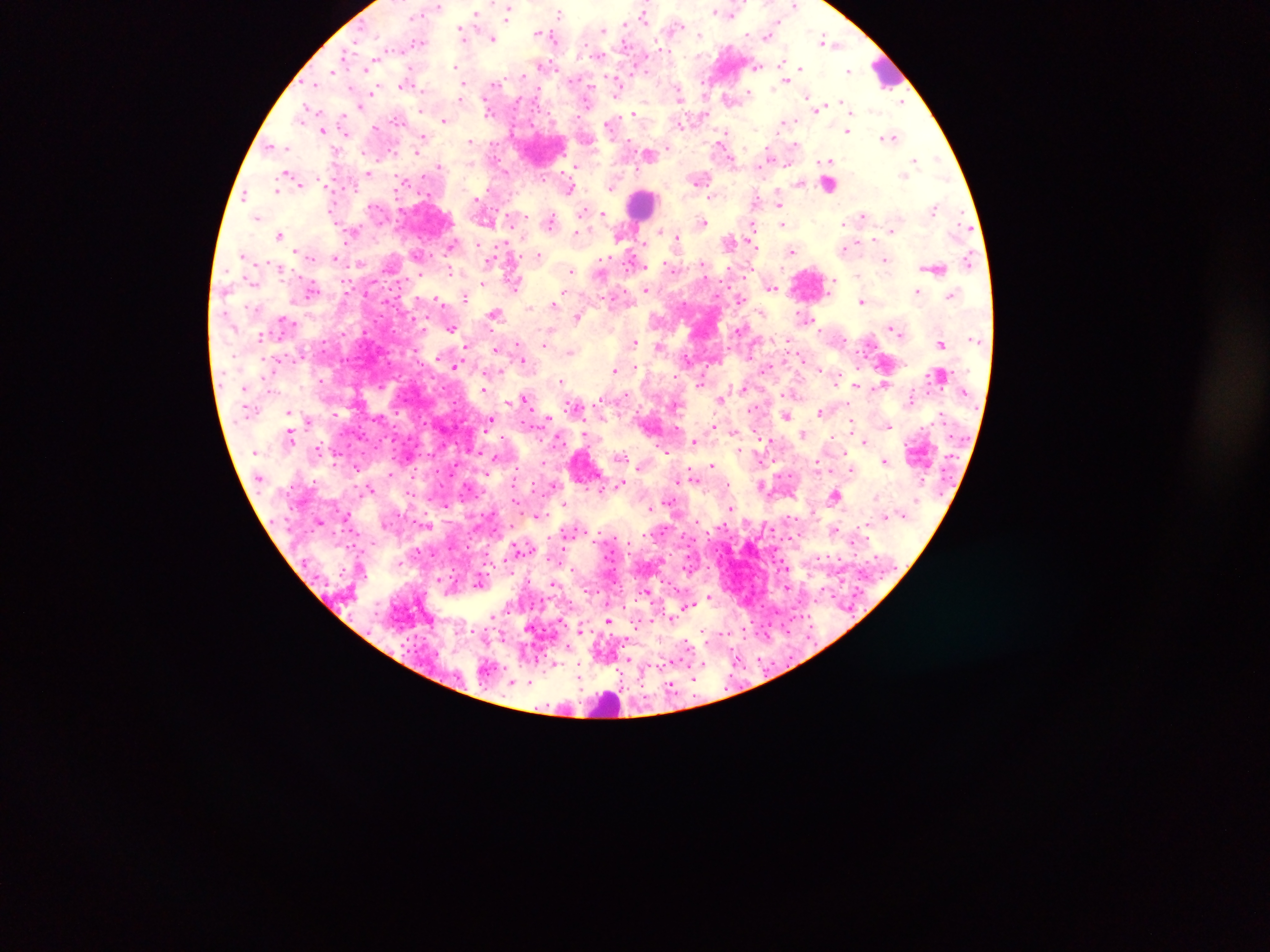
Approximate centers as (x, y) in pixels.
Summary:
  - Leukocyte locations: (886, 72), (643, 202), (607, 707)
  - Malaria parasite locations: (794, 6), (509, 12), (716, 12), (559, 13), (731, 13), (476, 14), (643, 15), (626, 23), (676, 26), (602, 29), (462, 31), (540, 33), (767, 34), (700, 35), (493, 38), (824, 39), (417, 42), (599, 55), (785, 61), (756, 66), (456, 67), (799, 68), (334, 70), (849, 70), (786, 80), (405, 83), (316, 84), (493, 86), (618, 86), (462, 88), (372, 92), (748, 93), (680, 95), (730, 99), (903, 102), (818, 107), (304, 111), (634, 113), (301, 117), (444, 120), (784, 122), (609, 124), (323, 130), (848, 130), (724, 134), (891, 137), (421, 139), (471, 141), (271, 146), (284, 148), (649, 154), (916, 160), (827, 161), (438, 165), (576, 166), (368, 172), (285, 173), (700, 178), (403, 183), (801, 183), (830, 185), (611, 187), (570, 189), (277, 191), (245, 195), (712, 197), (779, 202), (934, 208), (603, 213), (863, 215), (257, 218), (551, 220), (704, 221), (783, 224), (843, 225), (753, 227), (891, 231), (577, 233), (279, 235), (676, 236), (729, 241), (451, 245), (845, 248), (792, 251), (243, 255), (539, 255), (335, 258), (885, 260), (633, 262), (450, 271), (571, 271), (858, 275), (833, 281), (514, 284), (771, 287), (311, 289), (647, 290), (917, 291), (950, 295), (466, 297), (741, 299), (438, 300), (861, 301), (554, 304), (495, 314), (577, 317), (452, 328), (892, 328), (547, 336), (260, 338), (788, 340), (634, 342), (942, 344), (659, 347), (496, 350), (570, 351), (523, 358), (456, 366), (820, 368), (764, 369), (614, 370), (562, 381), (699, 384), (856, 385), (744, 388), (483, 389), (625, 394), (721, 398), (525, 400), (573, 405), (289, 412), (820, 412), (786, 416), (547, 417), (491, 420), (852, 420), (888, 425), (713, 426), (733, 431), (803, 434), (760, 439), (694, 442), (864, 442), (318, 448), (665, 450), (622, 456), (885, 461), (357, 466), (713, 466), (852, 471), (391, 473), (620, 483), (554, 485), (762, 486), (601, 489), (371, 490), (834, 495), (876, 497), (669, 502), (566, 504), (732, 508), (650, 509), (538, 515), (835, 529), (710, 597), (493, 616), (671, 618), (608, 620), (580, 628), (688, 645), (554, 663), (529, 683)
  - Image size: 1270×952 pixels
  - Field of view: single
  - Capture: mobile-phone photograph through a microscope
  - Preparation: thick blood film
  - Country: Ghana